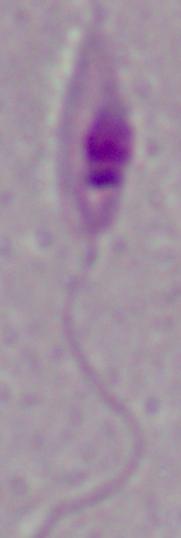
magnification = 1000x
identification = Leishmania
modality = micrograph